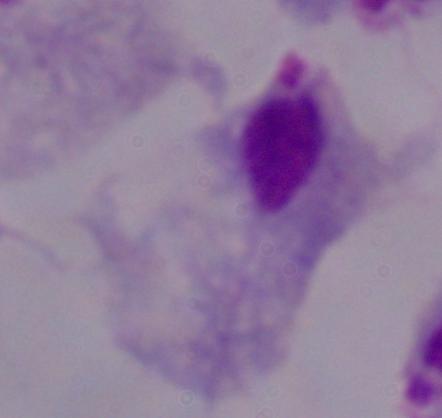

Summary:
  - Magnification: 1000x
  - Modality: micrograph
  - Identification: trichomonad